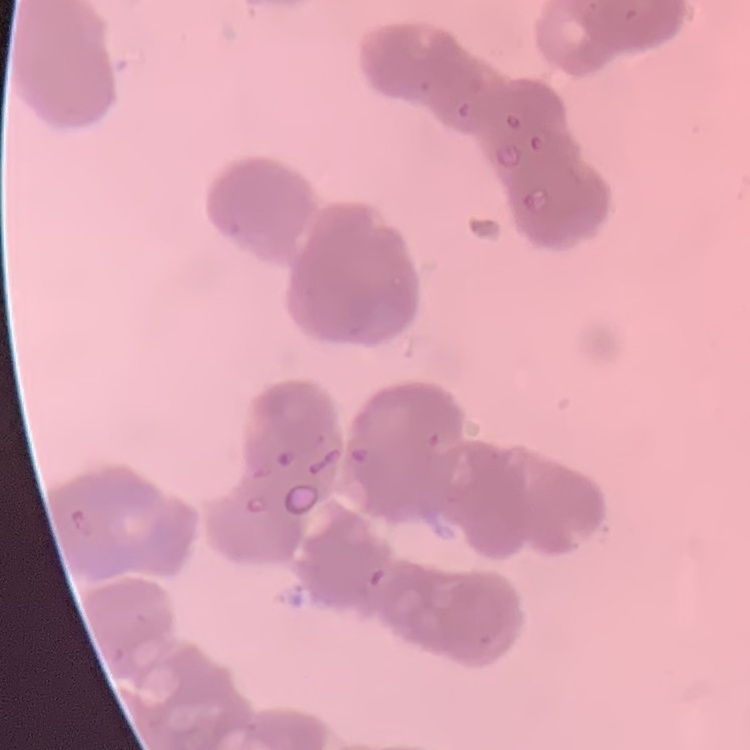

The red blood cells exhibit rouleaux formation. One tile cut from a larger photomicrograph. Field's or Giemsa stain. Thin peripheral smear.